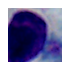 1000x magnification. A leukocyte is seen. Photomicrograph.